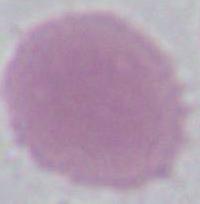

magnification = 1000x
modality = micrograph
identification = erythrocyte